Describe the morphology of the erythrocytes.
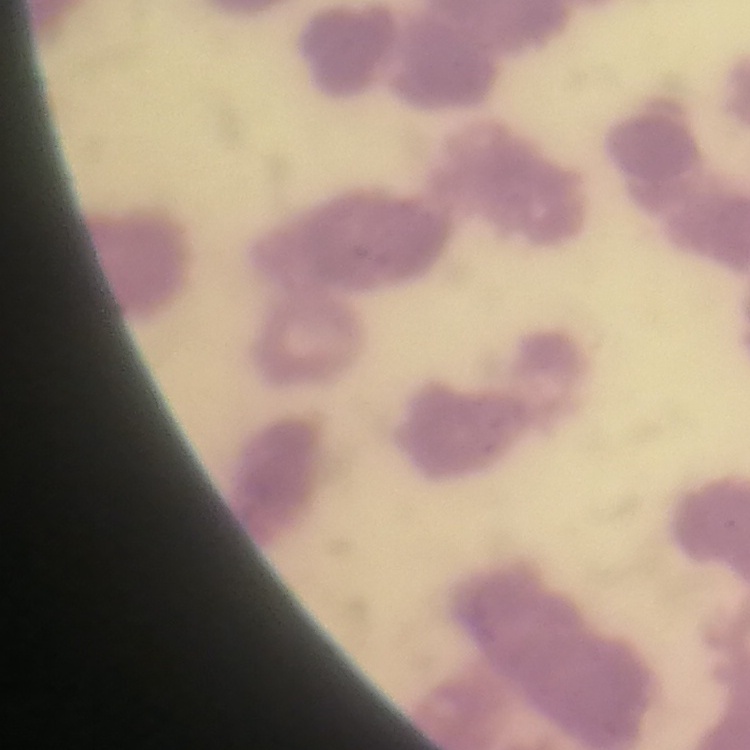

Rouleaux formation.

Stained with either Field's or Giemsa. Thin blood film. One tile cut from a larger photomicrograph.